Describe the morphology of the erythrocytes.
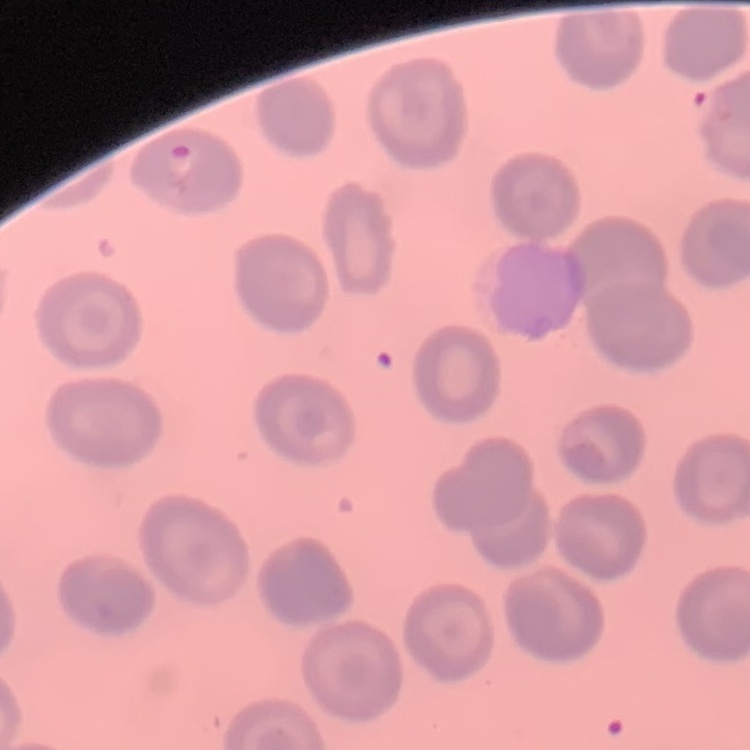

No rouleaux formation.

Square crop of a larger photomicrograph. Field's or Giemsa stain. Thin peripheral smear.